Report the malaria status of this cell.
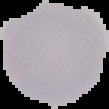
Uninfected.

image size = 109×109 pixels
image type = segmented cell region on a black background
preparation = thin blood smear